Assess this cell for malaria.
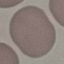
Uninfected.

Summary:
  - Preparation: thin blood film
  - Capture: smartphone camera at the microscope eyepiece
  - Stain: Giemsa
  - Image type: cell patch, automatically extracted from a larger field of view and resized to 64 × 64 pixels